Point out each malaria parasite.
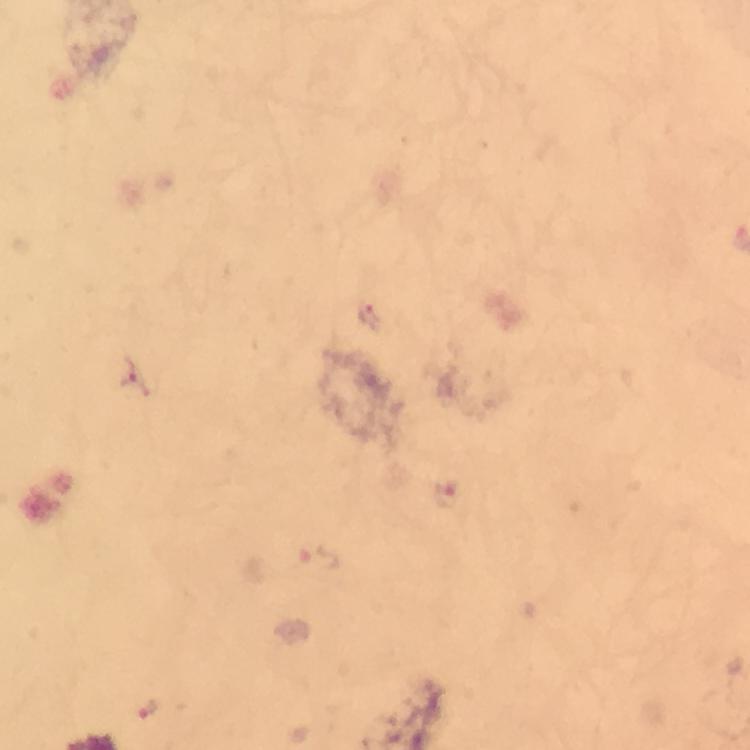

Approximate object centers, in pixels from the top-left corner.
Malaria parasites: (x=369, y=314), (x=129, y=375), (x=448, y=494), (x=317, y=560), (x=147, y=708).

Summary:
  - Preparation: thick blood film
  - Immersion oil: used
  - Magnification: 100x
  - Capture: smartphone mounted on the microscope
  - Image size: 750×750 pixels
  - Stain: Giemsa
  - Cropped from: a single field of view
  - Context: from a diagnostic examination for malaria